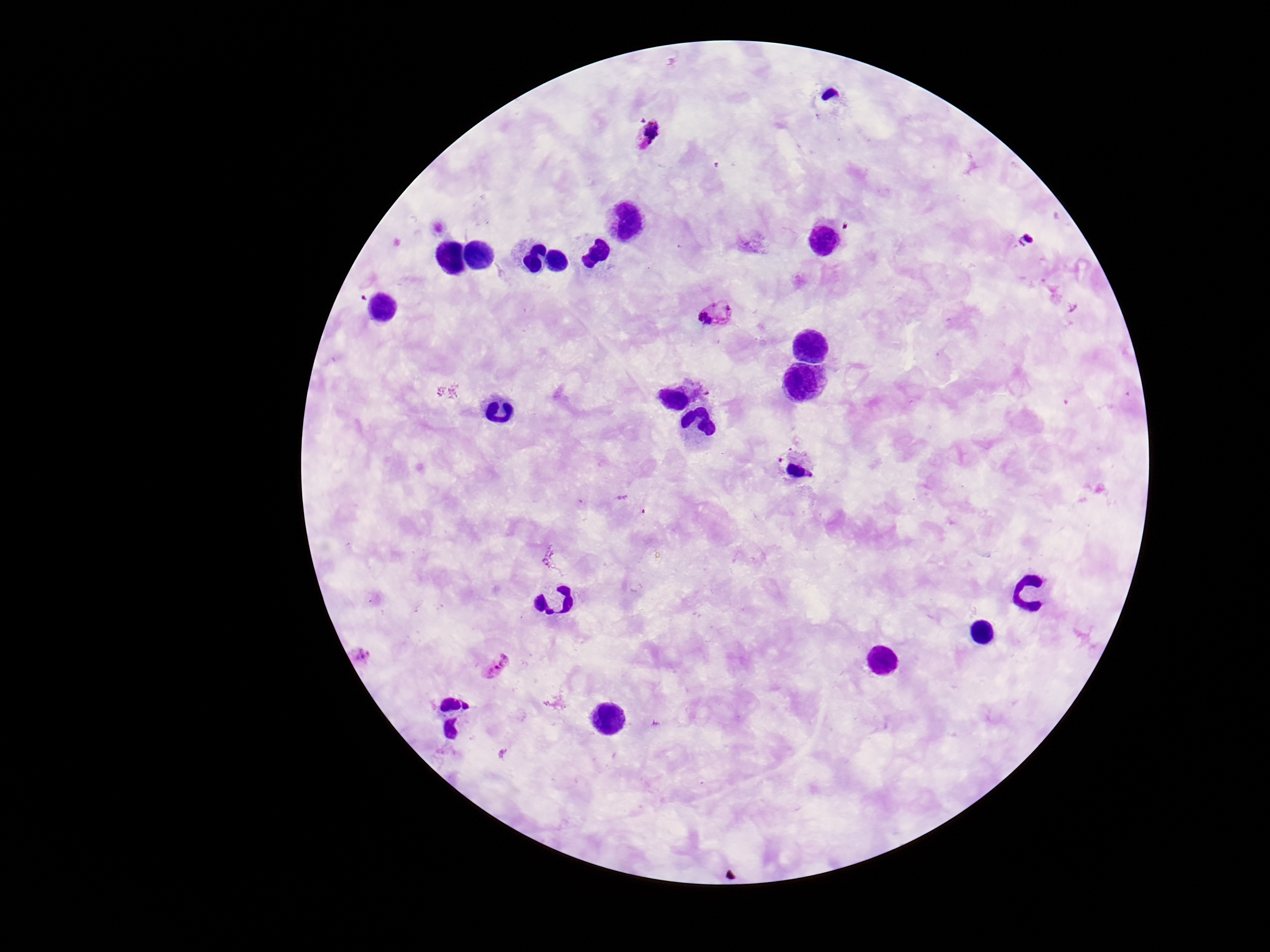 Approximate centers as {x, y} in pixels. Plasmodium parasite locations: {649, 133}, {718, 316}, {363, 654}, {495, 666}. Thick peripheral-blood smear. One field from this slide. Smartphone photograph taken through the microscope eyepiece. Image is 1270×952 pixels. Patient malaria status: positive. Giemsa-stained preparation. 100x magnification.